Assess the morphology of the red blood cells.
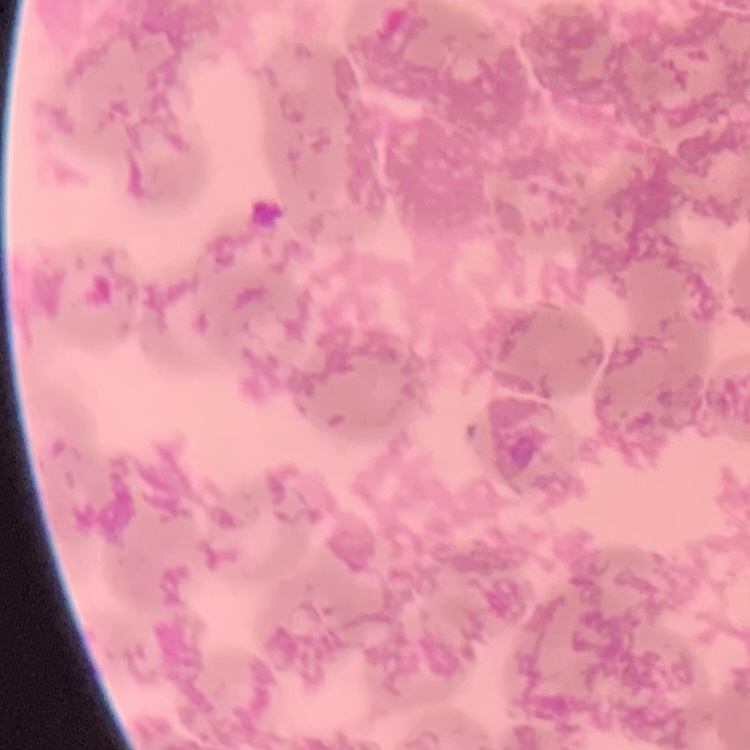

They show rouleaux formation.

stain = Field's or Giemsa
image type = one tile cut from a larger photomicrograph
preparation = thin blood film